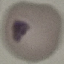

Summary:
  - Result: negative for malaria parasites
  - Preparation: thin blood film
  - Stain: Giemsa
  - Capture: smartphone camera at the microscope eyepiece
  - Image type: automatically extracted cell patch, resized to 64 × 64 pixels